State the blood parasite species.
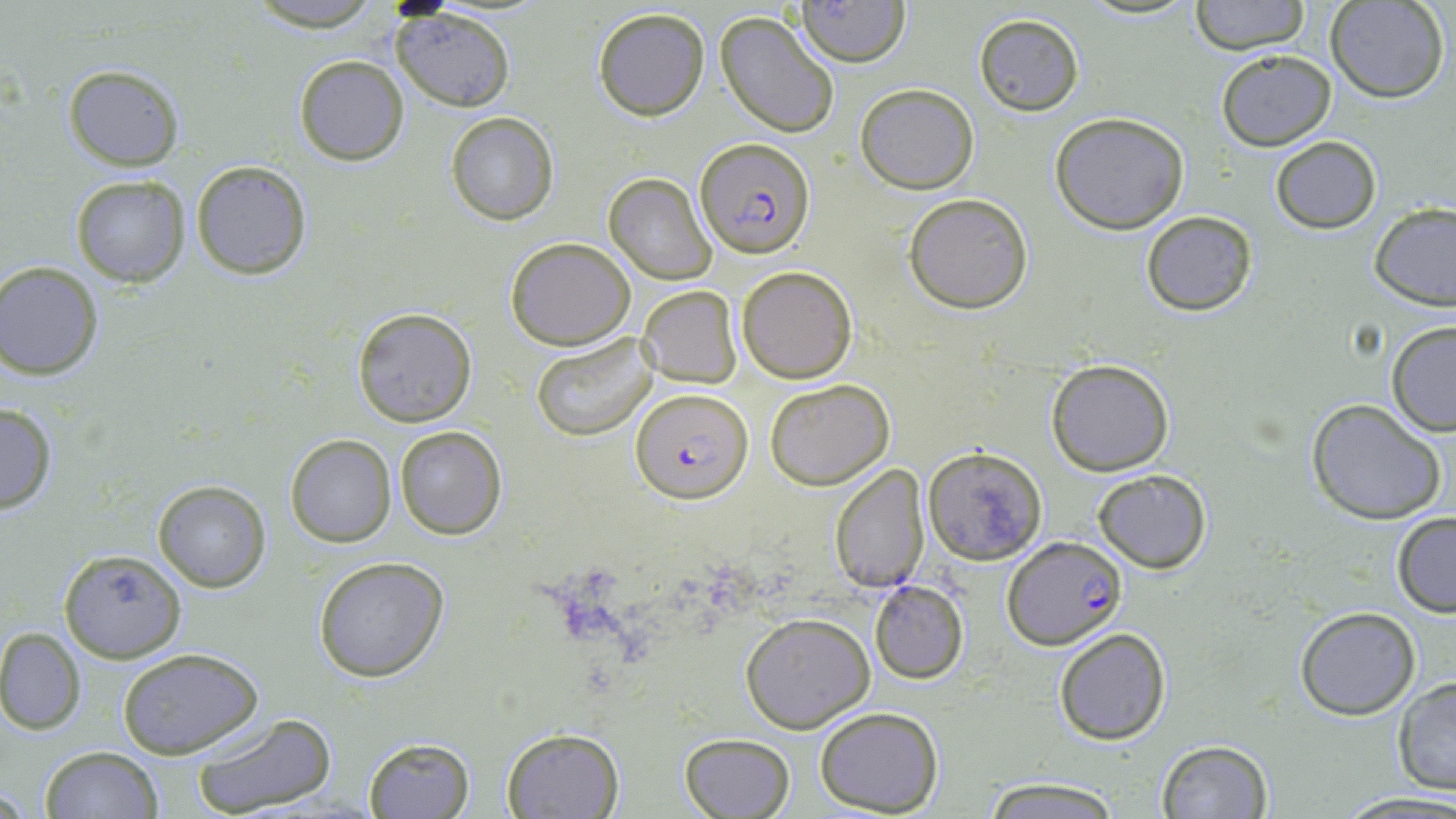

Plasmodium falciparum.

Approximate bounding boxes as (x1,y1)-(x2,y2) corner pairs in pixels. Plasmodium falciparum-infected red blood cell locations: (696,138)-(813,258), (632,387)-(752,505), (1001,535)-(1127,648). Uninfected red blood cell locations: (1188,0)-(1309,54), (1328,0)-(1449,103), (794,1)-(910,67), (241,3)-(390,31), (591,7)-(711,121), (392,9)-(516,112), (714,10)-(840,138), (972,12)-(1085,116), (1216,49)-(1336,151), (294,55)-(409,167), (63,65)-(184,170), (856,84)-(979,194), (446,112)-(559,225), (1049,112)-(1190,234), (1269,137)-(1382,233), (191,161)-(313,280), (604,173)-(717,285), (70,174)-(190,286), (24,192)-(147,335), (904,192)-(1033,313), (1370,203)-(1456,310), (1141,211)-(1257,316), (505,237)-(635,350), (0,261)-(104,380), (736,265)-(856,383), (637,286)-(741,385), (353,308)-(476,427), (1386,322)-(1456,437), (531,332)-(658,441), (1046,358)-(1174,476), (765,378)-(894,490), (1305,398)-(1448,524), (0,402)-(58,514), (394,425)-(506,539), (285,434)-(396,547), (923,446)-(1048,565), (829,464)-(929,594), (1092,469)-(1212,573), (152,480)-(270,591), (1391,510)-(1456,616), (59,549)-(187,662), (313,557)-(450,682), (869,580)-(969,684), (1294,607)-(1421,719), (740,612)-(876,732), (0,626)-(86,734), (1054,629)-(1172,745), (116,647)-(266,759), (1391,677)-(1456,795), (814,706)-(944,816), (189,712)-(339,819), (501,727)-(625,818), (679,733)-(796,819), (364,737)-(474,817), (1155,740)-(1272,819), (42,745)-(163,819), (977,777)-(1123,816), (1335,792)-(1456,817). Single field of view. 1000x magnification. Thin blood film. Optical microscopy. May-Grünwald-Giemsa stain. Image is 1456×819 pixels.